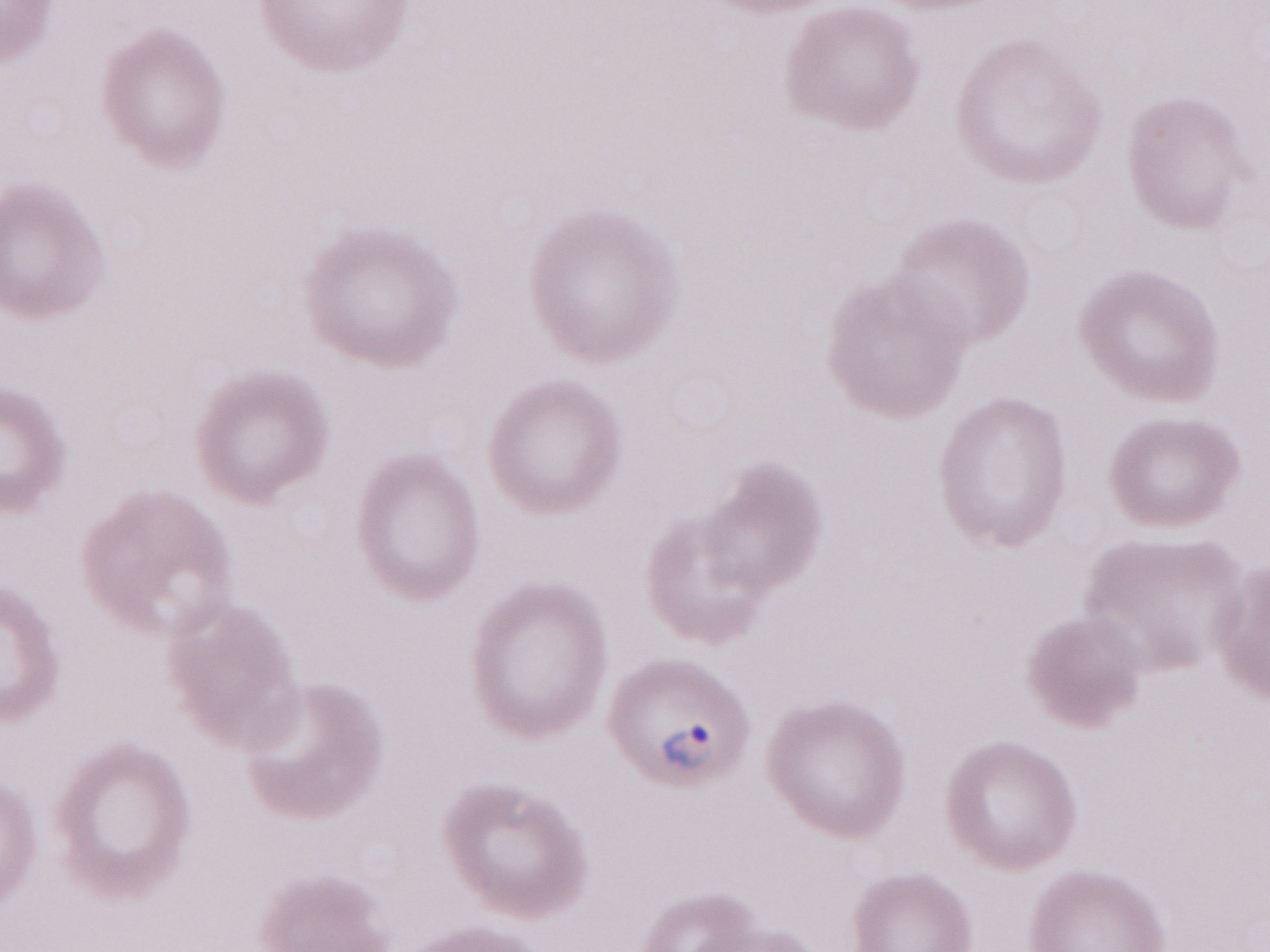 Patient diagnosis: malaria infection. Single field of view. May-Grünwald-Giemsa stain. Olympus BX43 microscope and DP73 digital camera. Image is 1270×952 pixels. Thin peripheral-blood smear. Magnification: 1,000x.